Describe the morphology of the erythrocytes.
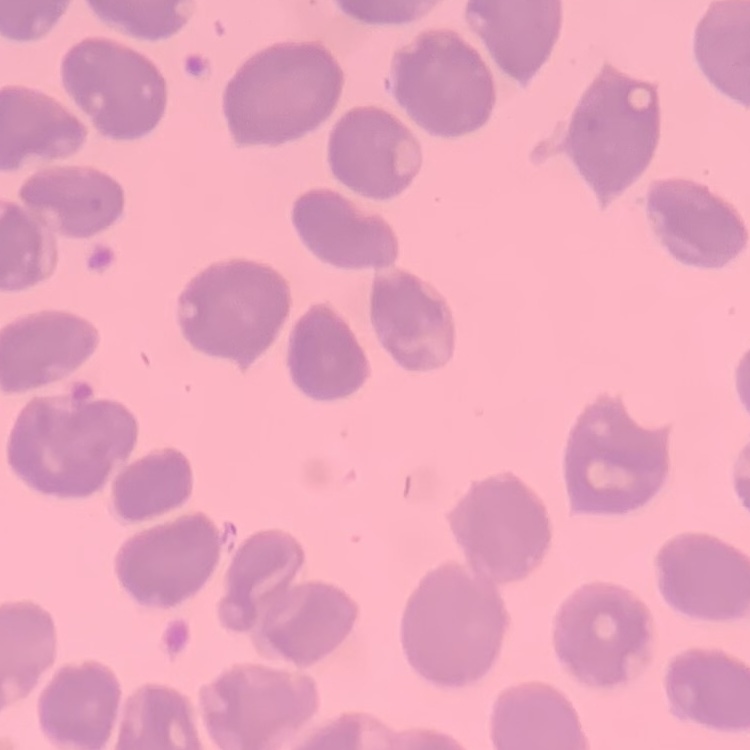

They show no rouleaux formation.

Stained with either Field's or Giemsa. Thin blood film. One tile cut from a larger photomicrograph.